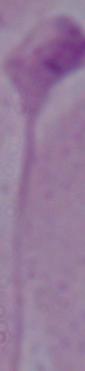
Summary:
  - Modality: photomicrograph
  - Identification: Leishmania
  - Magnification: 1000x